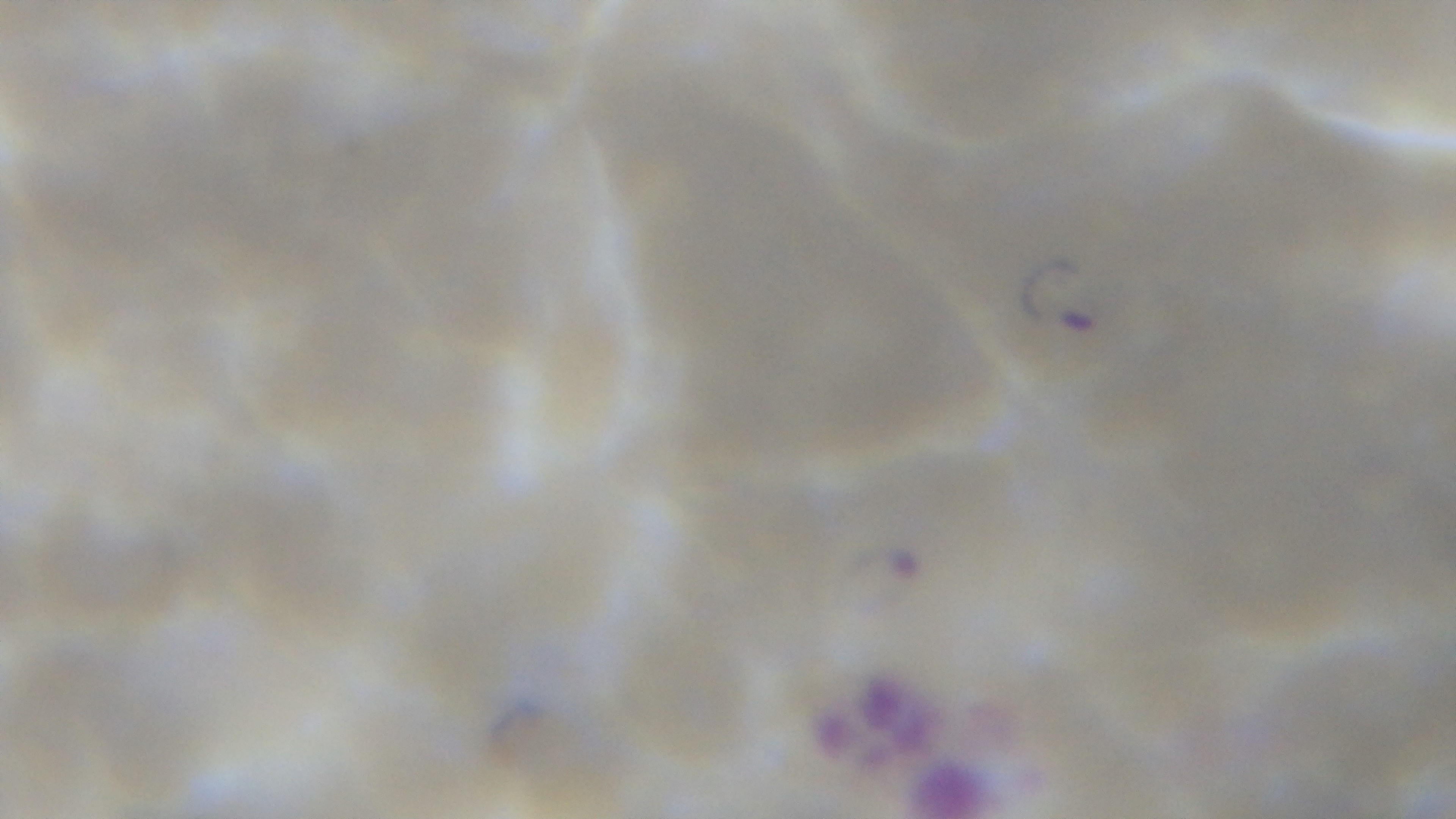
Single field of view. Light microscopy. Giemsa stain. Oil-immersion objective, 100x. Preparation: thin. Mounted 4K digital camera. Malaria status: positive.